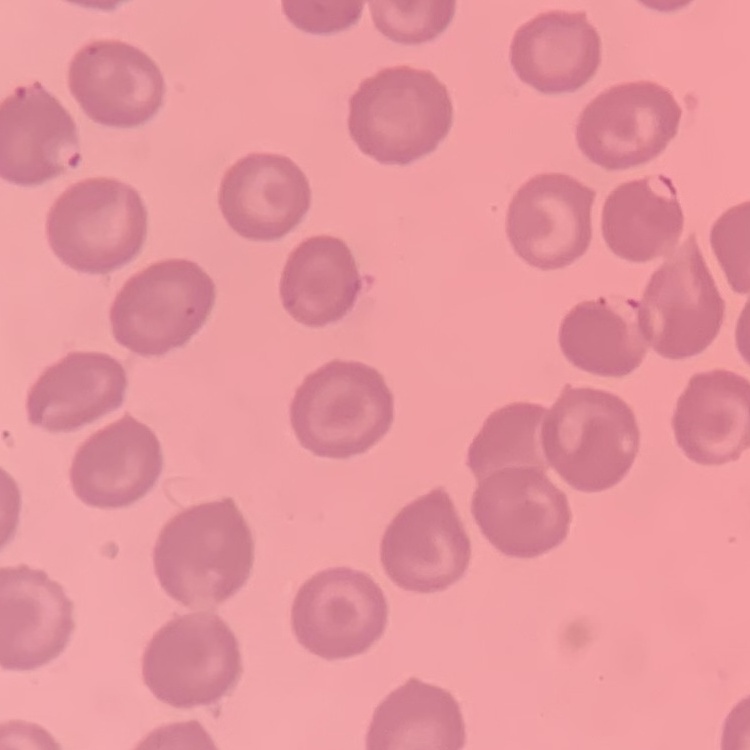
Summary:
  - Red blood cell morphology: no rouleaux formation
  - Stain: Field's or Giemsa
  - Image type: one tile cut from a larger photomicrograph
  - Preparation: thin peripheral smear